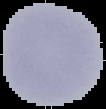 Cell region segmented out of the field of view; the surrounding area is masked to black. Result: negative for Plasmodium parasites. Image is 106×109 pixels. From a thin blood smear.